Classify this cell by malaria status.
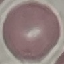

It is uninfected.

Summary:
  - Stain: Giemsa
  - Preparation: thin smear
  - Capture: smartphone through the microscope eyepiece
  - Image type: cell patch, automatically extracted from a larger field of view and resized to 64 × 64 pixels